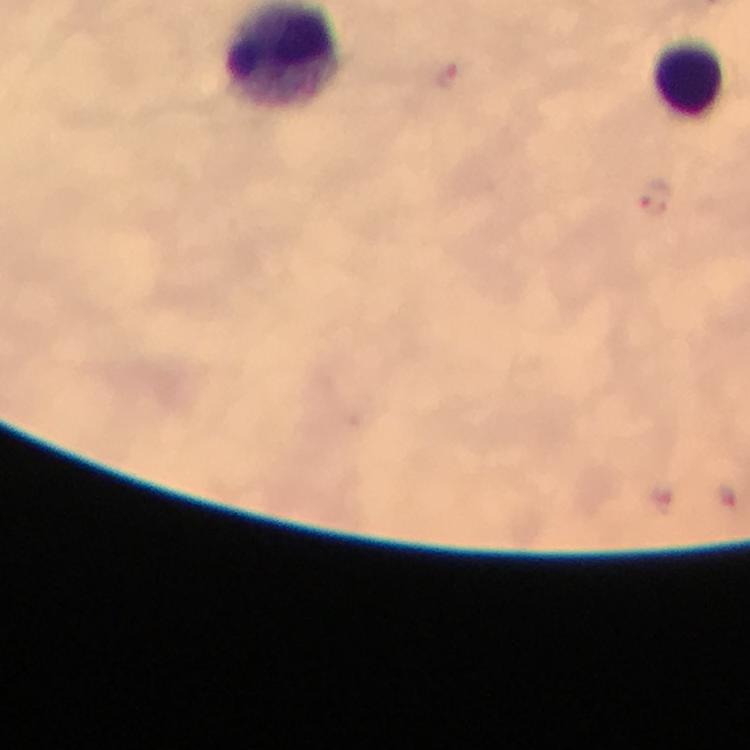

preparation = thick smear
malaria parasite locations = approximate centers as (x, y) in pixels: (446, 76), (653, 198)
context = from a diagnostic examination for malaria
magnification = 100x
immersion oil = applied
stain = Giemsa
cropped from = a single field of view
capture = smartphone camera through the microscope
leukocyte locations = approximate centers as (x, y) in pixels: (691, 74)
image size = 750×750 pixels